Give the position of every Plasmodium parasite.
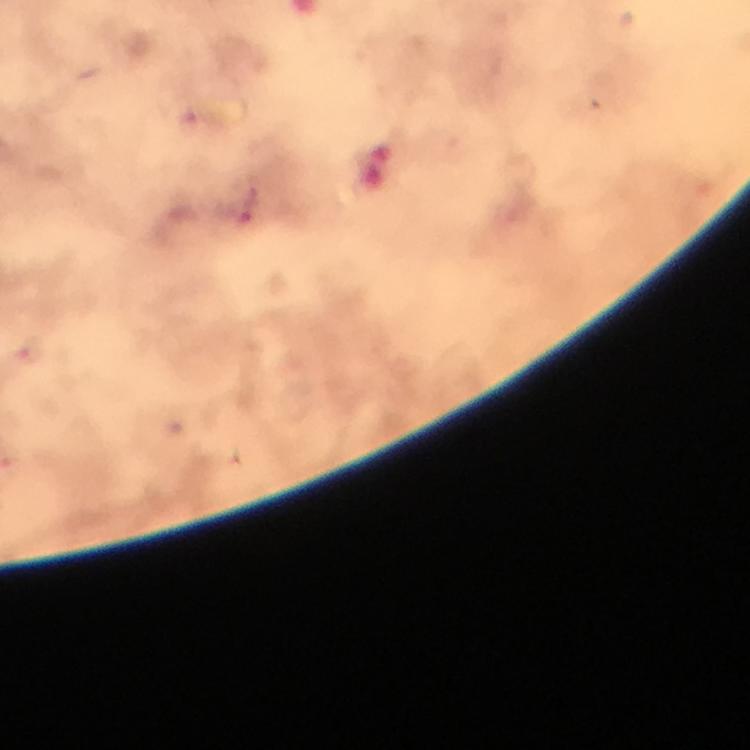

Approximate centers as (x, y) in pixels.
Plasmodium parasites: (248, 208).

immersion oil = used
image size = 750×750 pixels
preparation = thick smear
capture = smartphone camera through the microscope
stain = Giemsa
cropped from = a single field of view
magnification = 100x
context = from a malaria diagnostic workup